Assess this cell for malaria.
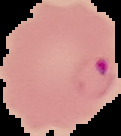
Parasitized.

Cell region segmented out of the field of view; the surrounding area is masked to black. Image is 121×136 pixels. From a thin blood smear.